Report the malaria status of this cell.
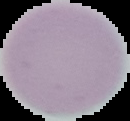

It is uninfected.

{
  "image_size": "130×121 pixels",
  "image_type": "cell region segmented out of the field of view; surrounding area masked to black",
  "preparation": "thin blood film"
}